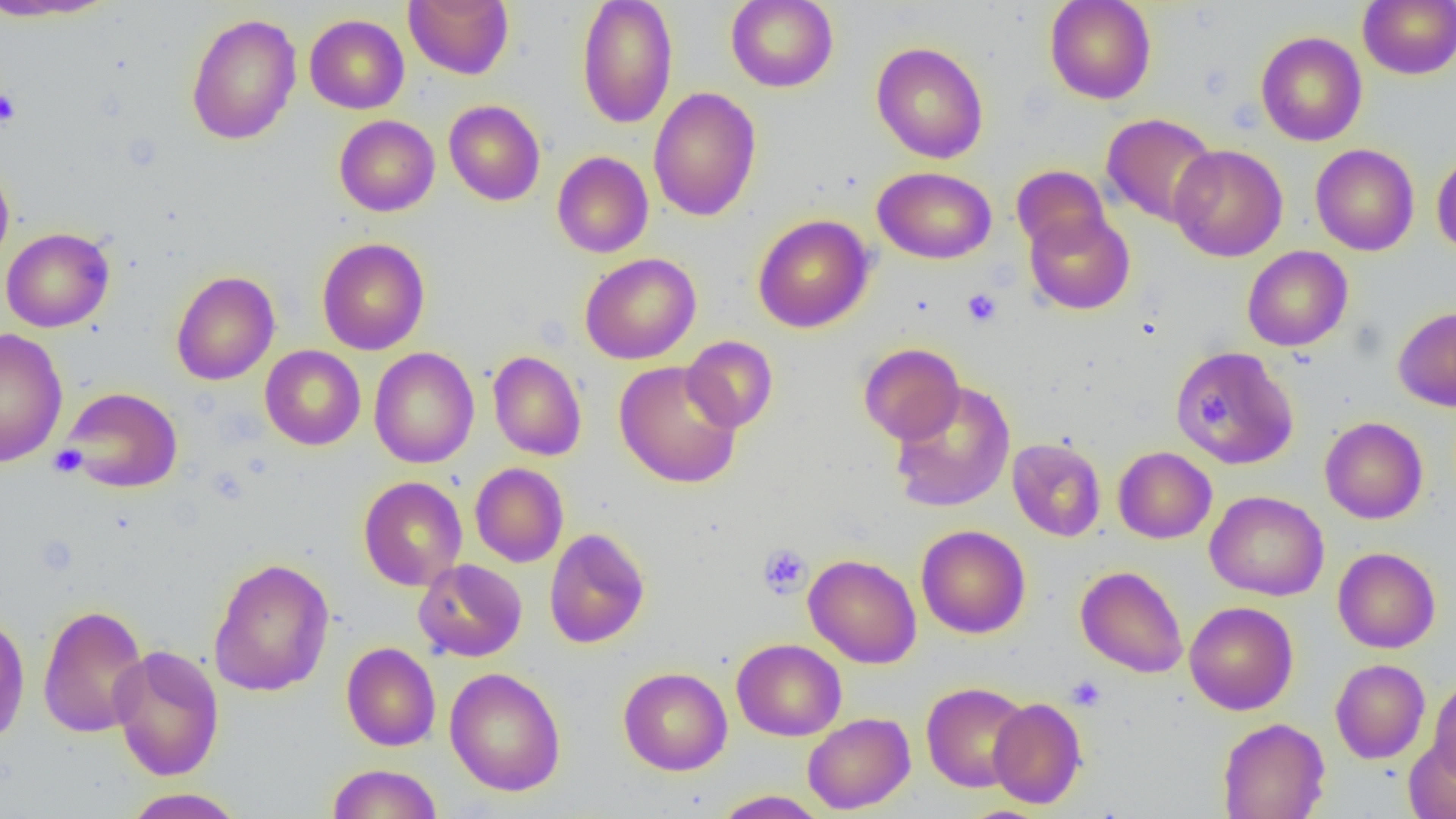 Approximate bounding boxes as (x1, y1, x2, y2) in pixels. Uninfected red blood cell locations: (0, 0, 119, 22), (404, 0, 514, 79), (576, 0, 678, 129), (726, 0, 838, 92), (1044, 0, 1157, 104), (1358, 0, 1456, 79), (186, 13, 302, 145), (304, 14, 409, 114), (1255, 31, 1367, 146), (871, 41, 988, 163), (648, 86, 762, 221), (444, 100, 545, 206), (1102, 113, 1219, 227), (334, 115, 440, 217), (1169, 144, 1288, 262), (1310, 144, 1419, 255), (1431, 150, 1456, 257), (552, 151, 653, 258), (0, 159, 14, 270), (1012, 165, 1110, 255), (872, 166, 997, 264), (1024, 210, 1135, 315), (753, 214, 874, 333), (1, 227, 114, 332), (316, 237, 430, 355), (1242, 246, 1352, 351), (579, 252, 701, 364), (171, 270, 280, 385), (1393, 306, 1456, 411), (0, 328, 67, 467), (681, 336, 778, 432), (858, 343, 965, 445), (260, 345, 366, 450), (1173, 346, 1299, 469), (368, 347, 479, 468), (488, 350, 586, 460), (613, 360, 744, 488), (889, 381, 1016, 513), (61, 386, 183, 493), (1319, 416, 1428, 524), (1007, 438, 1106, 541), (1113, 446, 1216, 543), (470, 463, 569, 567), (358, 476, 468, 591), (1205, 490, 1329, 601), (1195, 492, 1311, 713), (916, 525, 1031, 638), (543, 528, 650, 649), (1333, 547, 1441, 653), (804, 554, 921, 668), (208, 557, 335, 696), (414, 559, 528, 662), (1075, 565, 1188, 678), (1184, 601, 1298, 715), (38, 603, 149, 739), (0, 611, 30, 746), (732, 638, 846, 741), (341, 642, 440, 751), (110, 644, 225, 781), (1330, 659, 1430, 764), (618, 666, 732, 775), (445, 667, 566, 797), (1428, 675, 1456, 784), (921, 682, 1031, 792), (988, 698, 1087, 809), (802, 712, 915, 814), (1217, 717, 1330, 819), (1404, 738, 1456, 818), (326, 763, 443, 818), (121, 788, 245, 818), (712, 789, 829, 818). Platelet locations: (0, 88, 21, 128), (962, 288, 1002, 327), (1193, 399, 1228, 427), (49, 445, 87, 477), (757, 544, 812, 599), (1066, 675, 1107, 711). Slide-level diagnosis: negative for blood parasites. Thin blood film. Optical microscopy. Single field of view. Image is 1456×819 pixels. 1000x magnification.